Point out each malaria parasite.
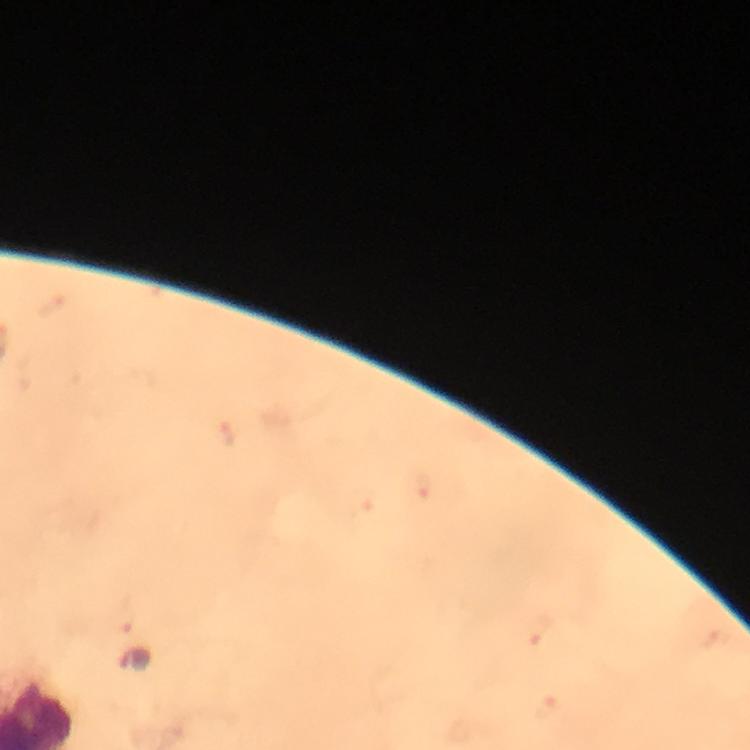

Approximate object centers, in pixels from the top-left corner.
Malaria parasites: (x=136, y=659).

Summary:
  - Image size: 750×750 pixels
  - Stain: Giemsa
  - Cropped from: a single field of view
  - Capture: smartphone mounted on the microscope
  - Immersion oil: applied
  - Magnification: 100x
  - Preparation: thick smear
  - Context: from a malaria diagnostic workup